Locate and identify every blood parasite.
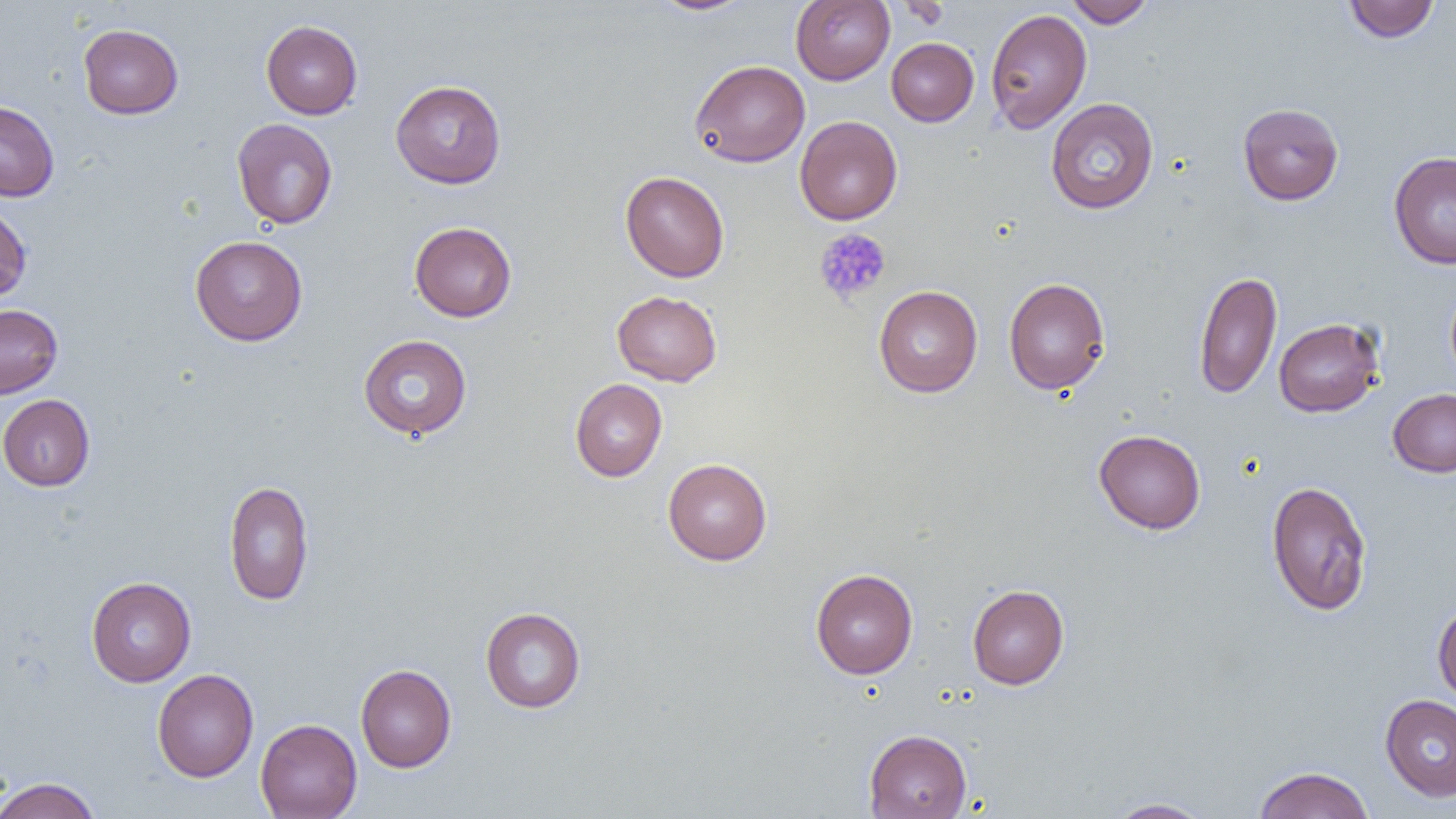

No blood parasites observed.

slide-level diagnosis = negative for blood parasites
image size = 1456×819 pixels
platelet locations = approximate bounding boxes as (x1, y1, x2, y2) in pixels: (813, 228, 891, 305)
magnification = 1000x
preparation = thin blood smear
field of view = one of a larger specimen
modality = optical microscopy
uninfected red blood cell locations = approximate bounding boxes as (x1, y1, x2, y2) in pixels: (650, 0, 756, 16), (790, 0, 894, 85), (1064, 0, 1156, 28), (1343, 0, 1440, 43), (897, 1, 952, 29), (985, 8, 1092, 133), (260, 20, 363, 119), (78, 24, 183, 119), (886, 37, 978, 126), (690, 60, 810, 167), (390, 79, 506, 189), (1045, 98, 1159, 214), (0, 100, 59, 201), (1238, 103, 1344, 205), (795, 115, 902, 225), (232, 118, 337, 229), (1388, 151, 1456, 269), (620, 171, 730, 282), (0, 203, 31, 302), (409, 221, 517, 322), (190, 235, 308, 346), (1194, 270, 1282, 400), (1003, 277, 1111, 395), (1445, 280, 1456, 387), (873, 285, 983, 397), (612, 290, 722, 386), (0, 304, 62, 399), (1273, 317, 1384, 417), (358, 334, 472, 439), (570, 378, 667, 482), (1388, 388, 1456, 477), (0, 394, 95, 491), (1094, 429, 1206, 534), (662, 458, 772, 565), (223, 479, 314, 606), (1265, 480, 1373, 617), (811, 568, 918, 679), (86, 576, 197, 686), (967, 584, 1069, 689), (1432, 602, 1456, 706), (480, 607, 586, 713), (355, 664, 457, 772), (152, 668, 258, 782), (1379, 694, 1456, 802), (255, 718, 362, 819), (863, 729, 972, 818), (1253, 766, 1374, 819), (0, 776, 102, 819), (1106, 798, 1213, 818)